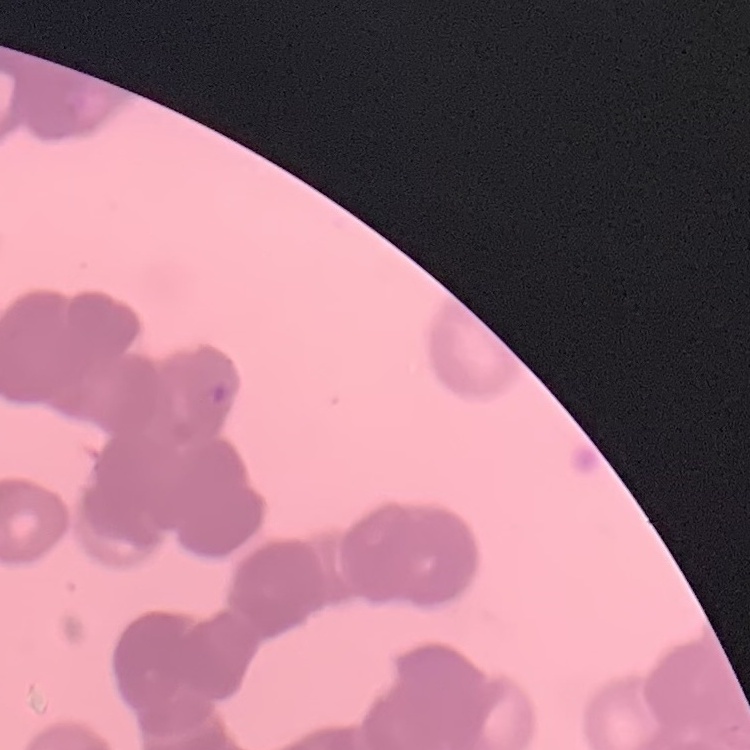

Summary:
  - Erythrocyte morphology: rouleaux formation
  - Stain: Field's or Giemsa
  - Preparation: thin blood film
  - Image type: square crop of a larger photomicrograph